Describe the morphology of the red blood cells.
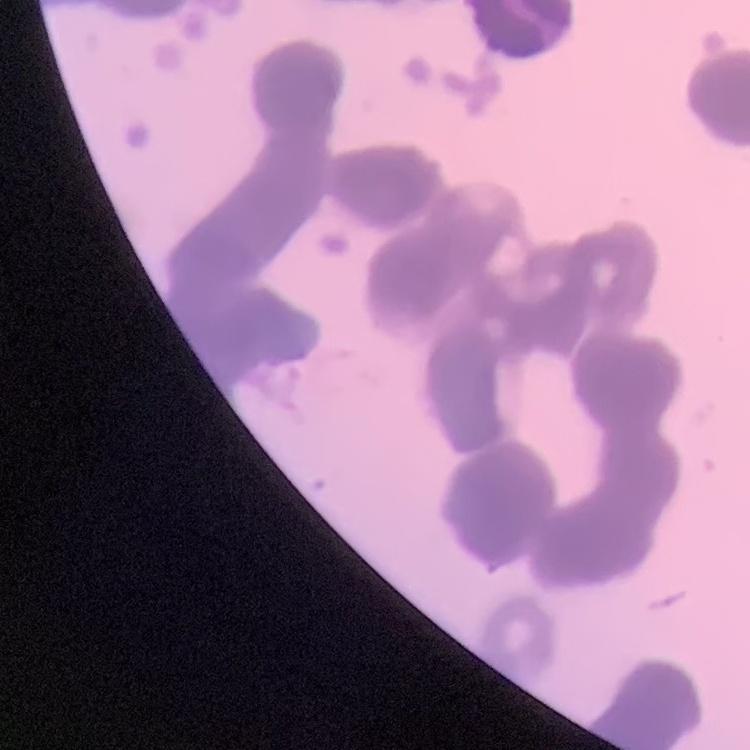

They show rouleaux formation.

Summary:
  - Preparation: thin peripheral smear
  - Stain: Field's or Giemsa
  - Image type: square crop of a larger photomicrograph